Report the malaria status of this cell.
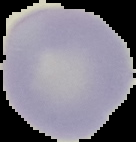
Uninfected.

From a thin blood smear. Image is 136×142 pixels. Segmented cell region on a black background.